Name the parasite shown.
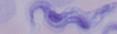
A trypanosome.

Summary:
  - Modality: photomicrograph
  - Magnification: 1000x